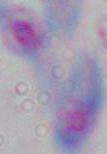

modality: micrograph
identification: Toxoplasma gondii
magnification: 1000x